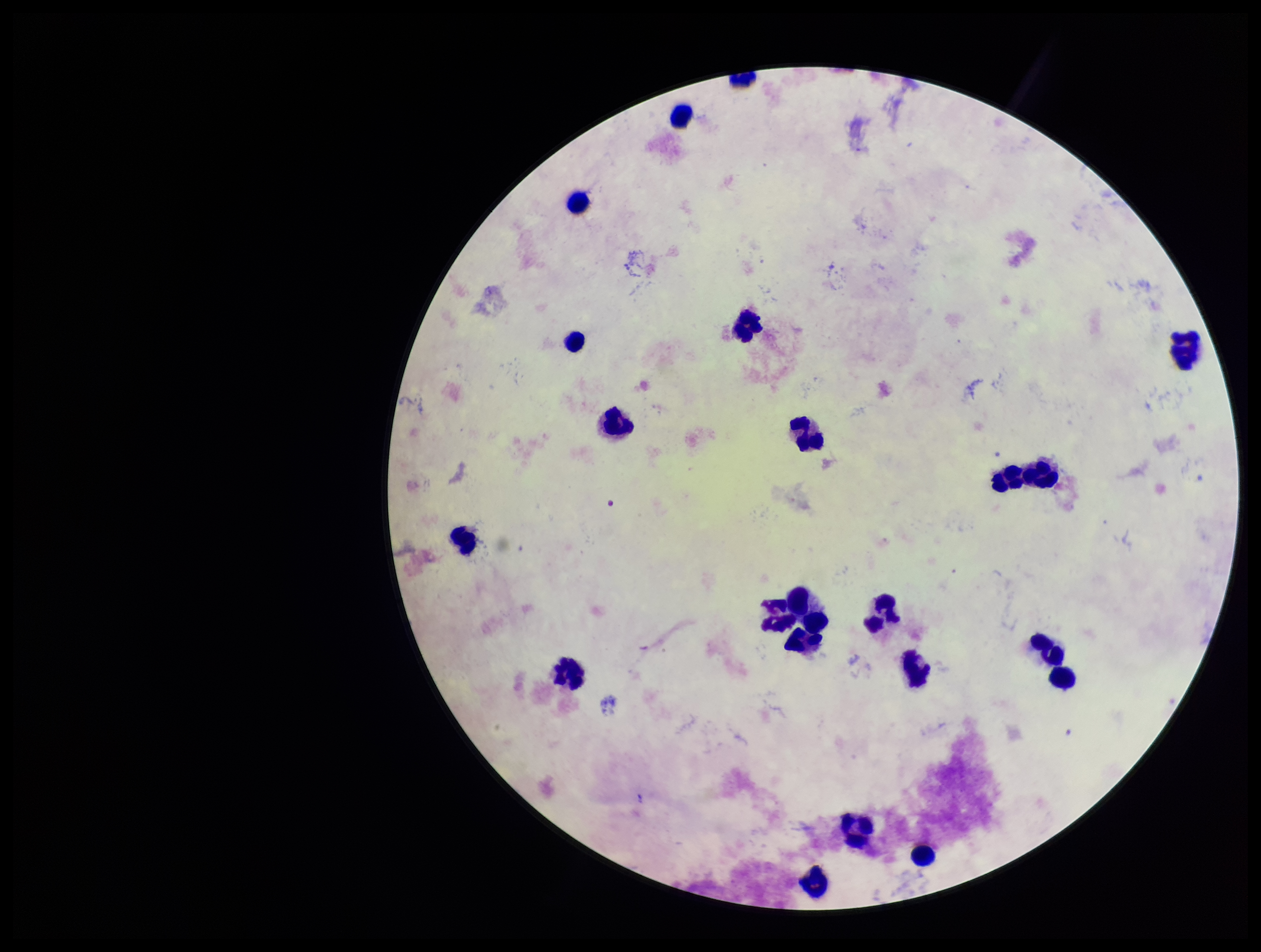
Preparation: thick blood smear. Single field of view. Leukocyte count: 22. Parasite count: 0. Plasmodium parasites: none detected. Photographed through the microscope eyepiece with a smartphone camera. Giemsa stain. Patient malaria status: negative. Image is 1261×952 pixels.